Assess the morphology of the erythrocytes.
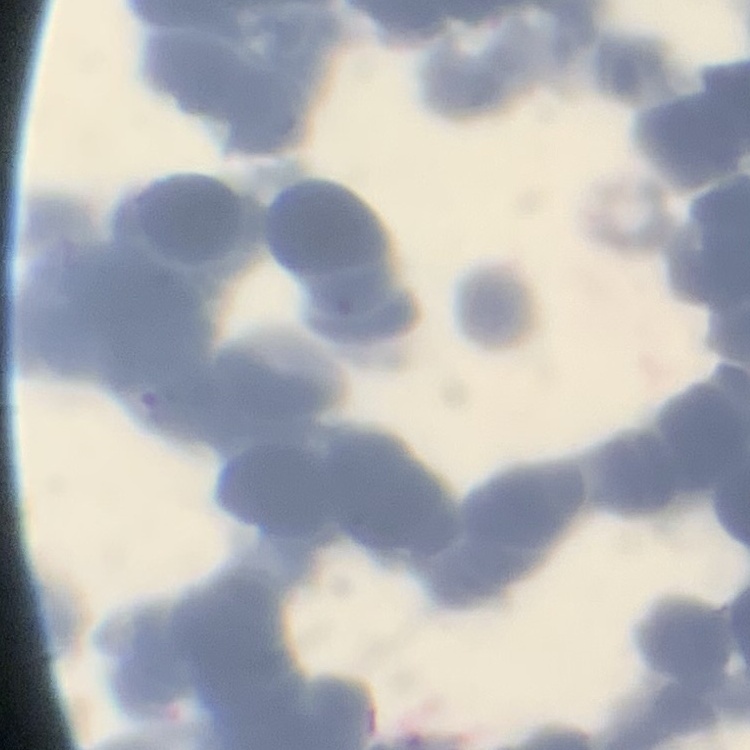
Rouleaux formation.

Thin blood film. Stained with either Field's or Giemsa. Square crop of a larger photomicrograph.